Name the cell type shown.
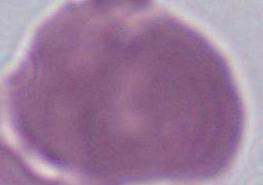

This is an erythrocyte.

1000x magnification. Photomicrograph.